Classify this cell by malaria status.
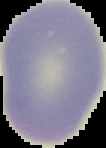
It is uninfected.

preparation: thin blood film
image_type: segmented cell region with the area outside set to black
image_size: 106×148 pixels